Comment on the morphology of the erythrocytes.
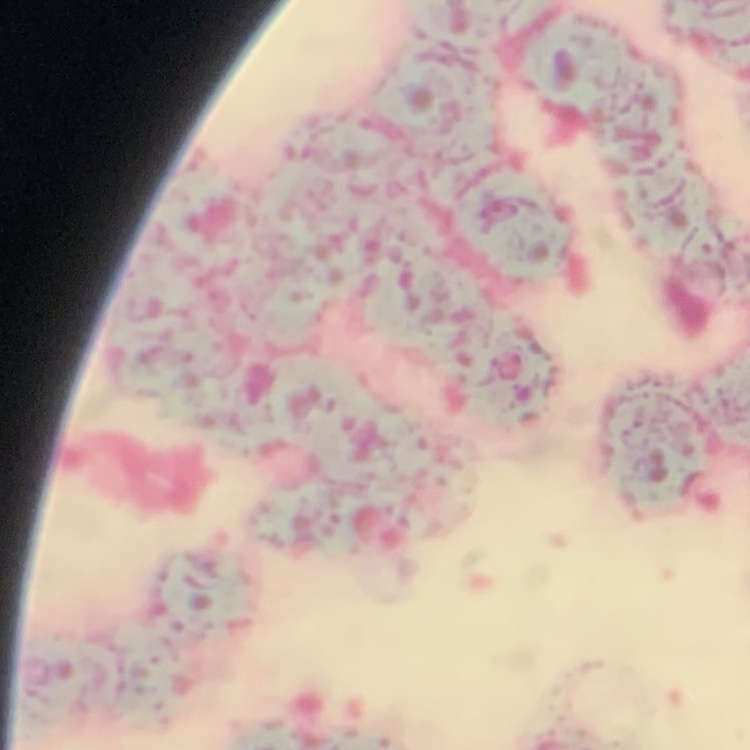
They show rouleaux formation.

Square crop of a larger photomicrograph. Field's or Giemsa stain. Thin blood smear.